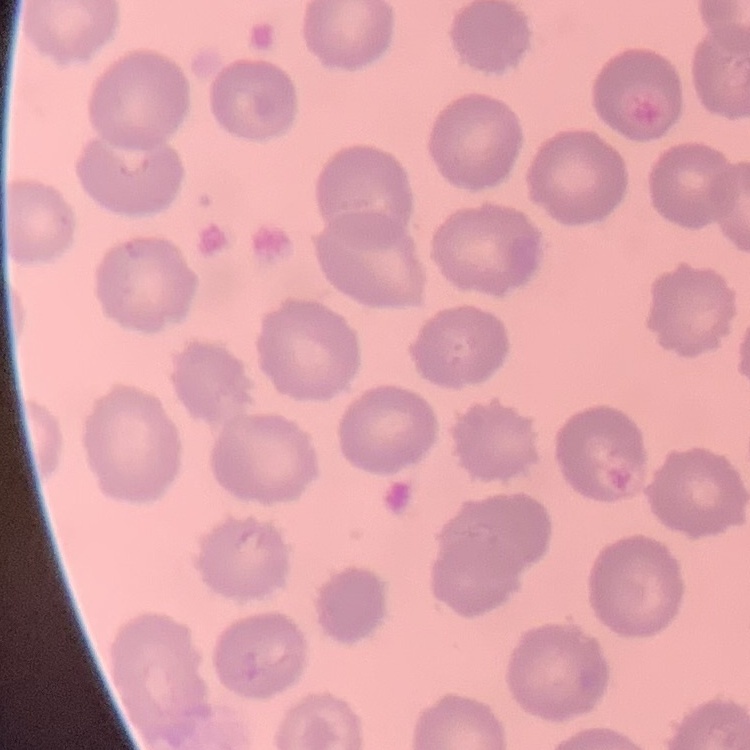 The erythrocytes show no rouleaux formation. One tile cut from a larger photomicrograph. Field's or Giemsa stain. Thin blood film.